Locate every uninfected red blood cell.
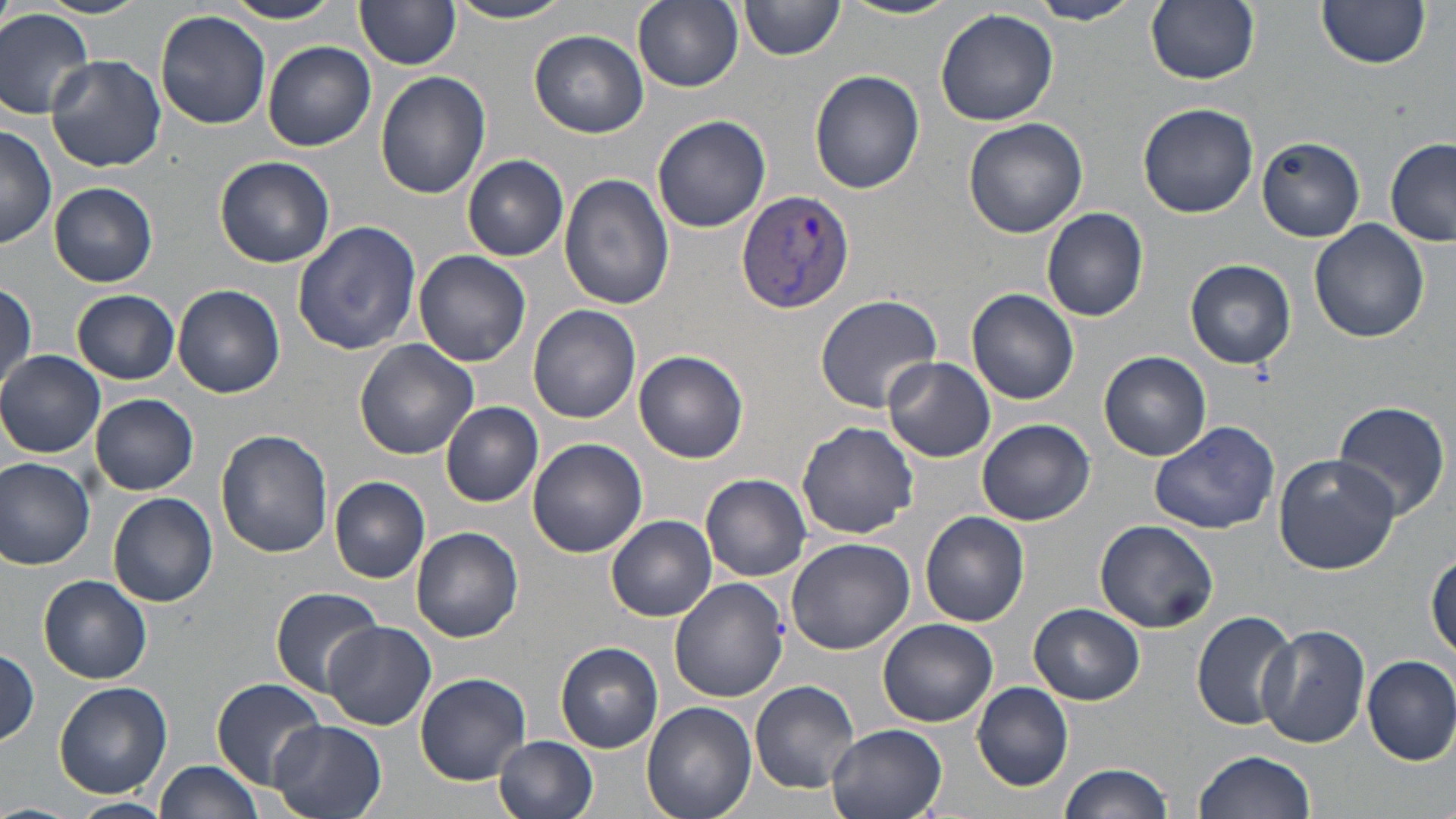

Approximate bounding boxes as [x1, y1, x2, y2] in pixels.
Uninfected red blood cells: [39, 0, 148, 19], [223, 0, 347, 25], [355, 0, 463, 70], [448, 0, 576, 24], [632, 0, 744, 91], [838, 0, 965, 20], [1145, 0, 1260, 86], [1316, 0, 1432, 69], [1026, 1, 1144, 25], [739, 2, 845, 63], [0, 8, 96, 119], [935, 8, 1059, 127], [155, 10, 272, 130], [529, 29, 649, 138], [263, 41, 376, 151], [45, 54, 167, 174], [810, 69, 925, 194], [375, 71, 492, 199], [1137, 102, 1258, 219], [652, 115, 771, 233], [963, 118, 1088, 239], [0, 125, 58, 249], [1256, 137, 1366, 241], [1385, 138, 1456, 246], [462, 155, 569, 261], [215, 156, 335, 268], [559, 172, 676, 311], [50, 182, 159, 287], [1041, 206, 1150, 322], [292, 219, 422, 356], [1309, 219, 1429, 343], [414, 249, 531, 368], [1185, 259, 1296, 369], [1, 283, 37, 397], [173, 285, 285, 398], [967, 288, 1079, 405], [72, 290, 180, 385], [814, 294, 943, 414], [529, 304, 641, 424], [354, 340, 477, 460], [0, 350, 106, 458], [634, 351, 749, 464], [1099, 352, 1211, 461], [881, 357, 995, 463], [89, 393, 200, 495], [1334, 400, 1454, 520], [442, 402, 544, 507], [976, 418, 1094, 526], [795, 420, 919, 539], [1148, 420, 1279, 535], [216, 429, 334, 557], [527, 438, 647, 557], [1272, 454, 1401, 574], [0, 456, 96, 570], [702, 473, 812, 580], [328, 475, 431, 583], [108, 492, 219, 609], [920, 511, 1030, 626], [606, 515, 718, 621], [1095, 520, 1221, 636], [410, 527, 523, 642], [784, 535, 915, 656], [1427, 551, 1456, 659], [40, 575, 152, 683], [670, 578, 788, 703], [269, 584, 385, 697], [1029, 603, 1144, 705], [1191, 610, 1301, 730], [879, 618, 998, 727], [320, 620, 436, 730], [1257, 624, 1371, 749], [555, 641, 664, 754], [0, 646, 41, 746], [1362, 654, 1456, 766], [414, 672, 531, 786], [212, 677, 328, 789], [54, 680, 172, 797], [749, 680, 861, 794], [972, 683, 1074, 791], [642, 702, 757, 819], [269, 720, 387, 819], [824, 722, 948, 819], [494, 736, 599, 819], [1192, 751, 1315, 819], [154, 760, 263, 818], [1058, 763, 1171, 819], [67, 796, 174, 818], [0, 802, 81, 819].

slide-level diagnosis = Plasmodium vivax
magnification = 1000x
field of view = single
preparation = thin blood smear
image size = 1456×819 pixels
Plasmodium vivax-infected red blood cell locations = approximate bounding boxes as [x1, y1, x2, y2] in pixels: [735, 189, 853, 315]
stain = May-Grünwald-Giemsa
modality = light microscopy